Name the parasite shown.
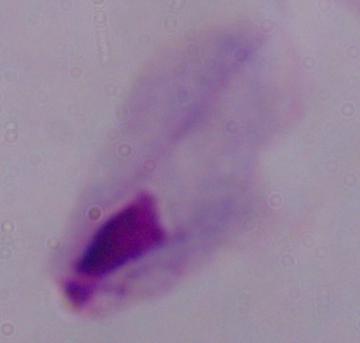

This is a trichomonad.

magnification = 1000x
modality = photomicrograph